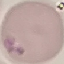

result = no malaria parasites seen
preparation = thin smear
image type = automatically extracted cell patch, resized to 64 × 64 pixels
capture = smartphone camera at the microscope eyepiece
stain = Giemsa